Name the parasite shown.
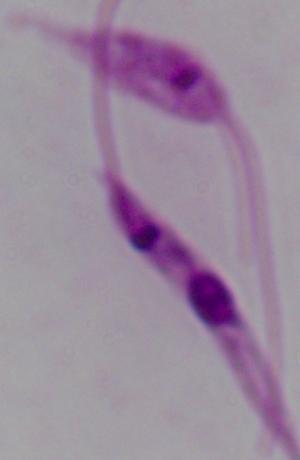
This is Leishmania.

magnification = 1000x
modality = micrograph